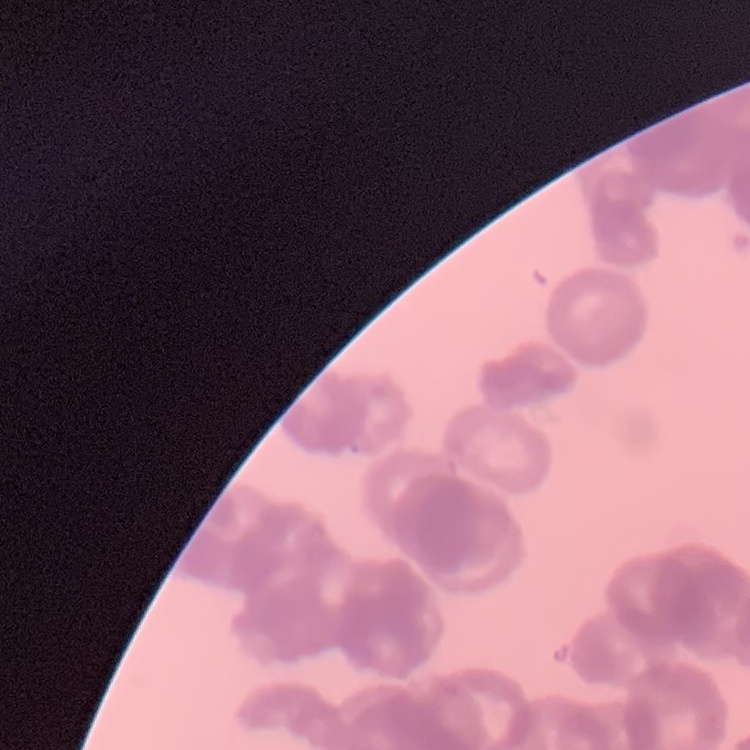

red blood cell morphology = rouleaux formation
stain = Field's or Giemsa
preparation = thin blood film
image type = square crop of a larger photomicrograph